Assess this cell for malaria.
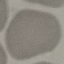
It is uninfected.

Summary:
  - Stain: Giemsa
  - Capture: smartphone through the microscope eyepiece
  - Image type: cell patch, automatically extracted from a larger field of view and resized to 64 × 64 pixels
  - Preparation: thin blood smear